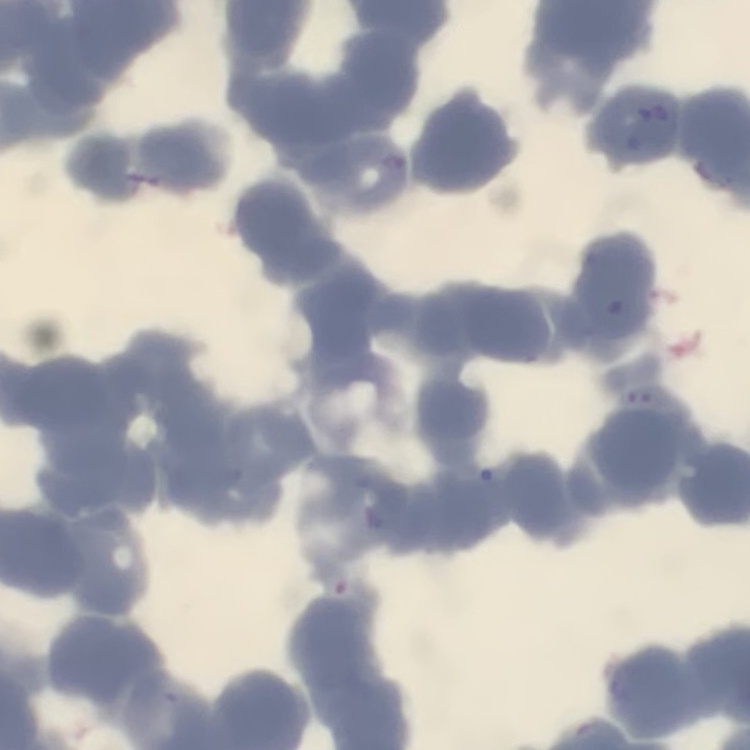

Summary:
  - Erythrocyte morphology: rouleaux formation
  - Image type: square crop of a larger photomicrograph
  - Preparation: thin peripheral smear
  - Stain: Field's or Giemsa